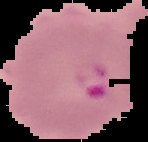

From a thin blood smear. Result: Plasmodium parasites identified. Image is 148×142 pixels. Segmented cell region on a black background.